Classify this cell by malaria status.
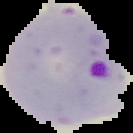

It is parasitized.

{
  "image_type": "cell region segmented out of the field of view; surrounding area masked to black",
  "preparation": "thin blood film",
  "image_size": "133×133 pixels"
}